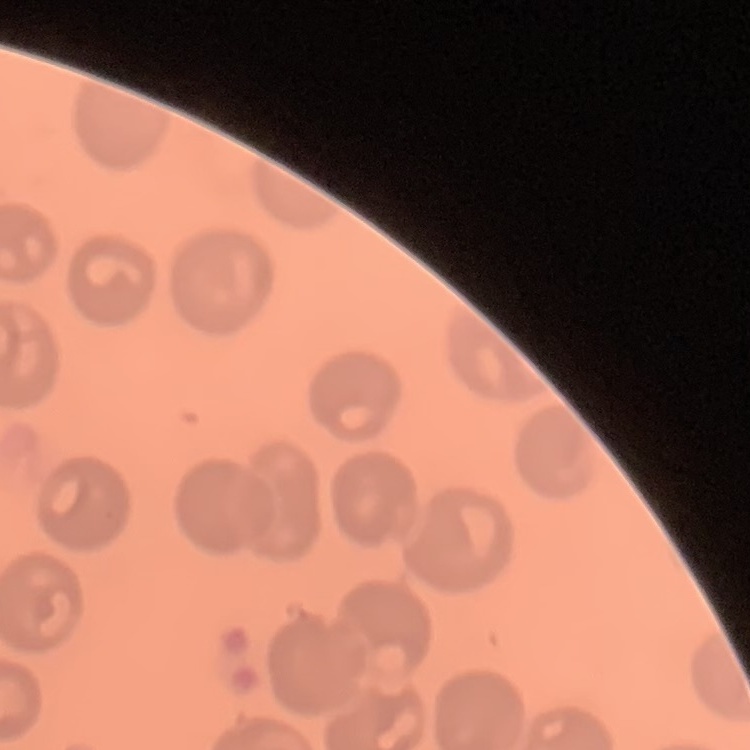

Summary:
  - Red blood cell morphology: no rouleaux formation
  - Image type: square crop of a larger photomicrograph
  - Stain: Field's or Giemsa
  - Preparation: thin blood smear